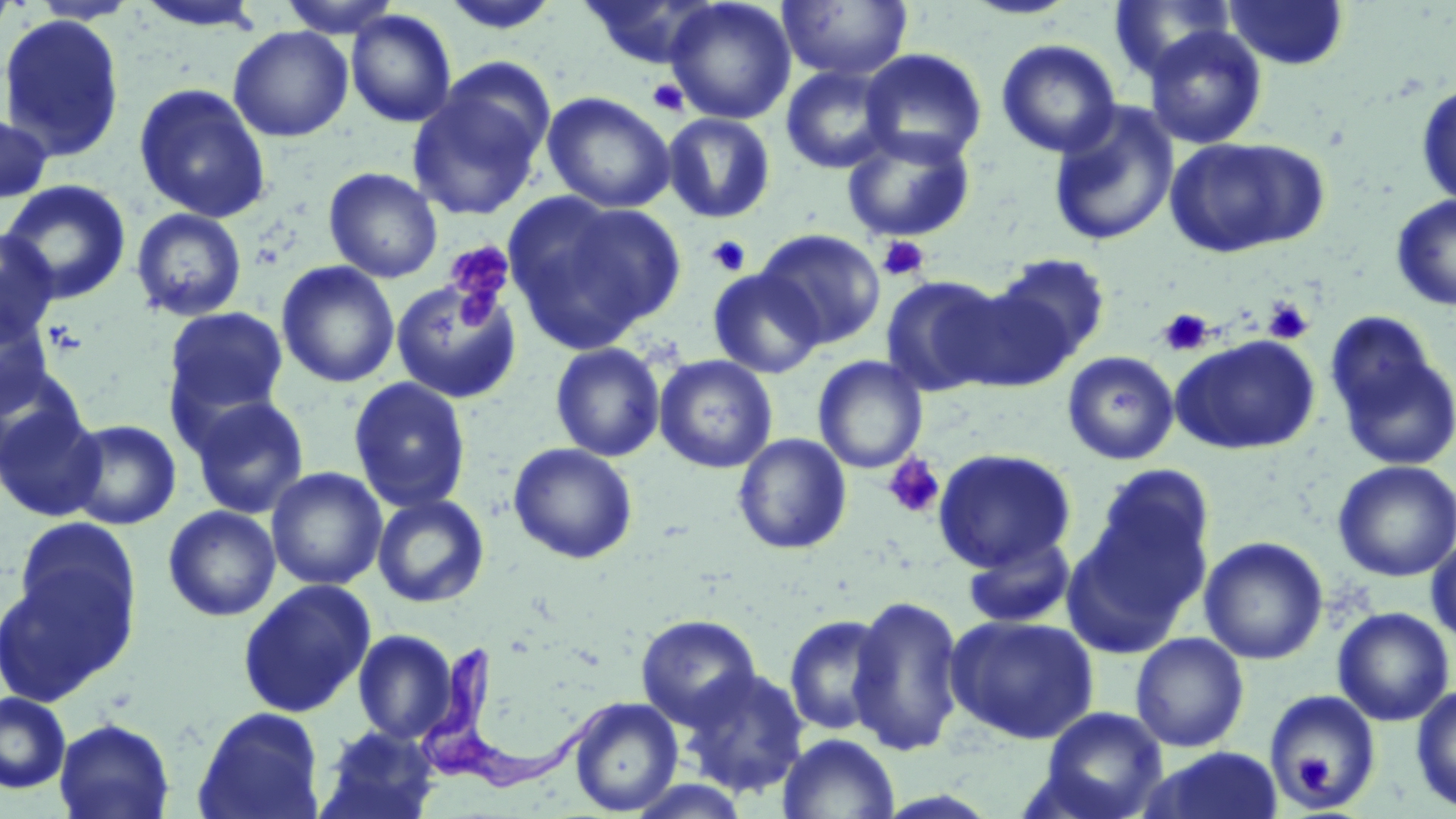

slide-level diagnosis = Trypanosoma brucei
preparation = thin blood film
stain = May-Grünwald-Giemsa
magnification = 1000x
field of view = one of a larger specimen
Trypanosoma brucei locations = approximate bounding boxes as [x1, y1, x2, y2] in pixels: [418, 643, 617, 795]
modality = light microscopy
uninfected red blood cell locations = approximate bounding boxes as [x1, y1, x2, y2] in pixels: [0, 0, 19, 45], [278, 0, 403, 38], [438, 0, 563, 34], [580, 0, 721, 70], [665, 0, 797, 124], [1109, 0, 1235, 82], [1223, 0, 1350, 70], [131, 1, 268, 33], [777, 1, 914, 82], [346, 9, 458, 128], [0, 14, 126, 163], [1142, 25, 1267, 150], [228, 26, 353, 142], [996, 39, 1121, 158], [860, 48, 987, 166], [780, 64, 898, 174], [407, 73, 551, 222], [1415, 81, 1456, 208], [133, 82, 272, 223], [543, 92, 675, 213], [1047, 102, 1180, 248], [0, 111, 54, 205], [662, 112, 777, 224], [841, 127, 976, 244], [1164, 135, 1327, 259], [323, 167, 443, 283], [1, 179, 132, 305], [1390, 194, 1456, 311], [506, 195, 684, 352], [130, 208, 248, 322], [0, 227, 60, 345], [755, 228, 886, 349], [988, 252, 1111, 370], [276, 260, 400, 388], [708, 268, 825, 378], [881, 274, 1007, 396], [390, 277, 521, 404], [942, 277, 1082, 393], [0, 304, 55, 419], [162, 306, 290, 426], [1326, 319, 1454, 471], [1170, 335, 1319, 455], [549, 342, 666, 462], [1062, 351, 1179, 465], [654, 355, 777, 474], [813, 356, 927, 474], [0, 362, 89, 473], [348, 377, 471, 513], [187, 395, 311, 519], [1, 402, 106, 521], [65, 414, 311, 522], [64, 419, 182, 530], [733, 433, 852, 555], [508, 442, 638, 564], [932, 447, 1077, 572], [1332, 460, 1456, 582], [1089, 463, 1215, 594], [266, 467, 387, 590], [372, 493, 490, 608], [163, 505, 281, 622], [1063, 508, 1207, 654], [13, 515, 142, 652], [962, 532, 1077, 630], [1426, 535, 1456, 648], [1199, 536, 1328, 664], [0, 558, 135, 706], [236, 578, 377, 718], [847, 593, 966, 757], [1332, 606, 1455, 727], [636, 613, 761, 729], [945, 613, 1099, 744], [784, 614, 891, 736], [352, 629, 460, 744], [1130, 632, 1249, 752], [681, 666, 810, 797], [1411, 685, 1456, 813], [1263, 690, 1382, 811], [0, 691, 72, 793], [569, 697, 683, 815], [192, 706, 326, 819], [1036, 706, 1168, 819], [53, 717, 175, 819], [314, 725, 441, 819], [777, 732, 900, 819], [1142, 746, 1285, 819]
image size = 1456×819 pixels
platelet locations = approximate bounding boxes as [x1, y1, x2, y2] in pixels: [647, 78, 689, 116], [706, 235, 752, 277], [877, 236, 929, 281], [443, 241, 515, 325], [1262, 296, 1313, 344], [1157, 309, 1214, 357], [882, 453, 946, 519], [1295, 752, 1335, 795]